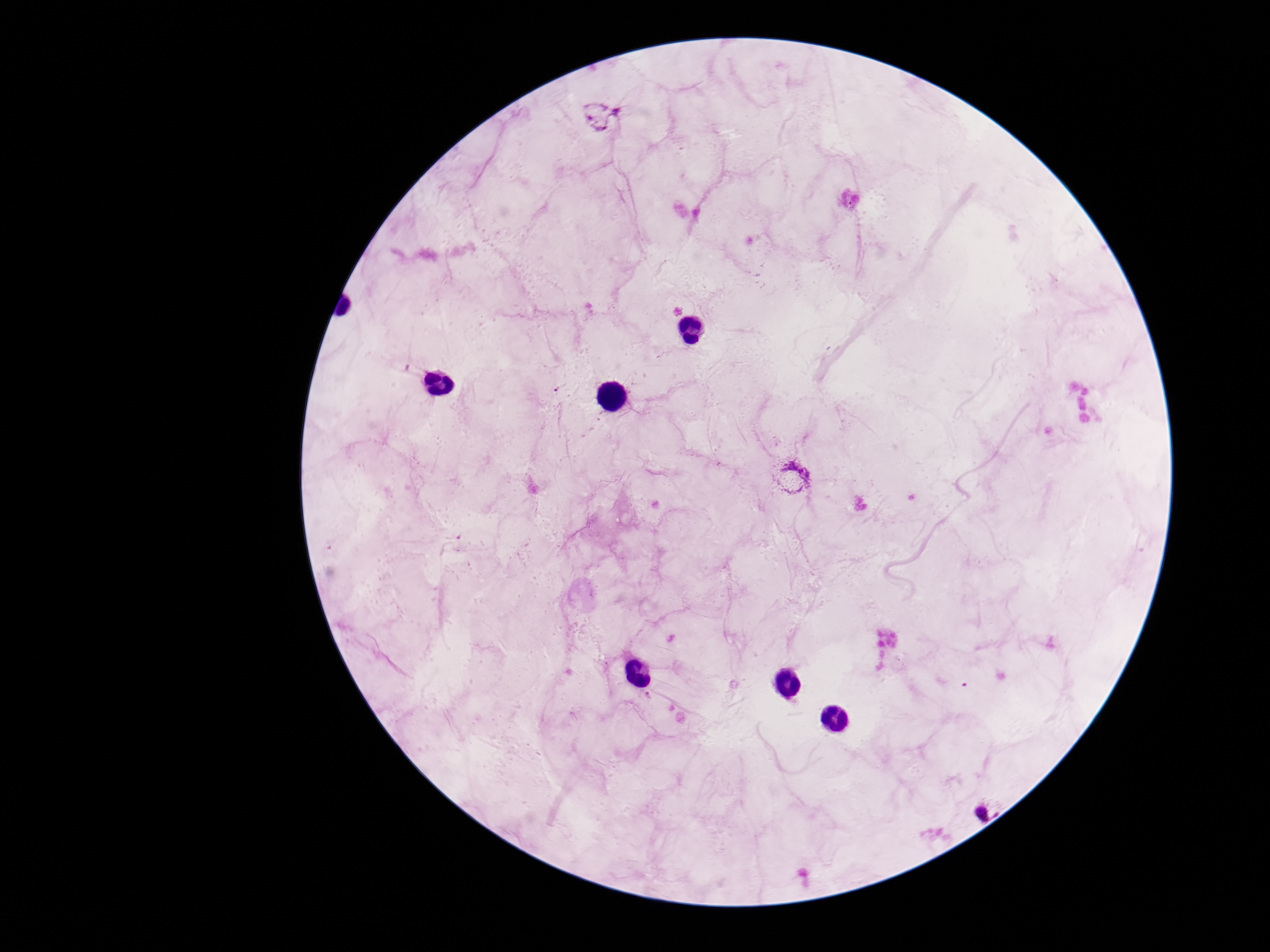

Approximate centers as (x, y) in pixels. Plasmodium parasite locations: (600, 117), (793, 476), (991, 804). Smartphone photograph taken through the microscope eyepiece. Image is 1270×952 pixels. Single field of view. Patient malaria status: positive. Giemsa-stained preparation. 100x magnification. Thick peripheral-blood smear.